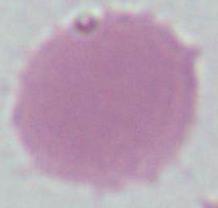

{
  "identification": "red blood cell",
  "modality": "photomicrograph",
  "magnification": "1000x"
}